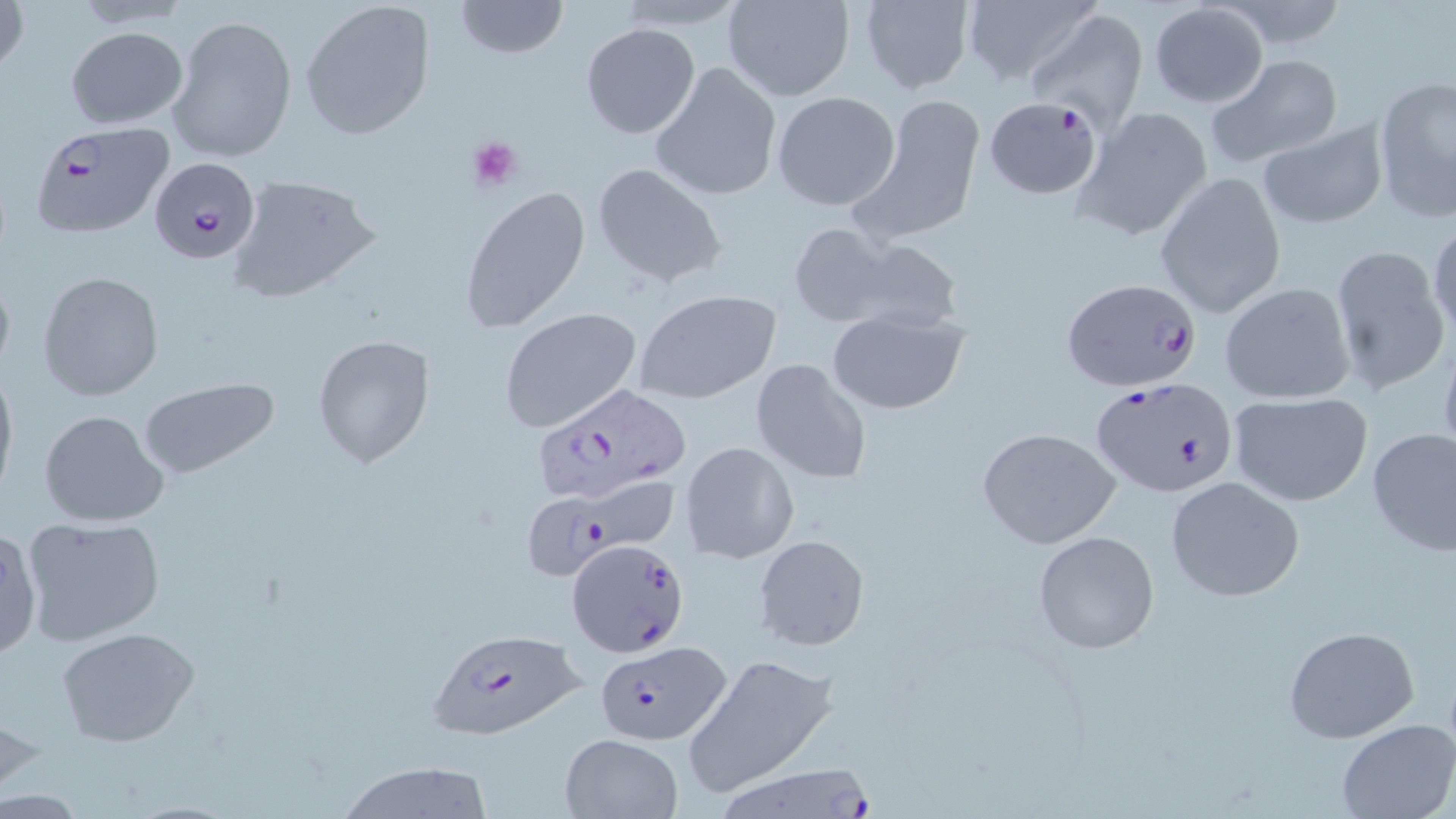
slide_level_diagnosis: Plasmodium falciparum
field_of_view: single
stain: May-Grünwald-Giemsa
image_size: 1456×819 pixels
plasmodium_falciparum_infected_red_blood_cell_locations: 'approximate bounding boxes as (x1, y1, x2, y2) in pixels: (983, 97, 1103, 200), (26, 122, 174, 240), (149, 157, 259, 264), (1060, 276, 1203, 392), (1089, 376, 1238, 498), (529, 385, 690, 506), (524, 482, 680, 590), (567, 539, 688, 659), (425, 628, 587, 741), (596, 641, 728, 741), (709, 764, 875, 818)'
magnification: 1000x
platelet_locations: 'approximate bounding boxes as (x1, y1, x2, y2) in pixels: (467, 134, 524, 193)'
preparation: thin blood smear
uninfected_red_blood_cell_locations: 'approximate bounding boxes as (x1, y1, x2, y2) in pixels: (0, 0, 29, 80), (298, 0, 438, 142), (722, 0, 855, 102), (858, 0, 975, 94), (959, 0, 1101, 89), (455, 1, 568, 58), (611, 2, 754, 33), (1147, 2, 1269, 108), (1027, 9, 1147, 127), (168, 15, 297, 162), (579, 23, 701, 139), (65, 26, 189, 130), (1205, 53, 1344, 168), (649, 61, 782, 202), (1371, 72, 1456, 225), (771, 91, 901, 212), (858, 96, 985, 238), (1073, 105, 1213, 240), (1256, 119, 1389, 232), (591, 163, 727, 289), (226, 172, 382, 305), (1156, 172, 1286, 320), (461, 184, 590, 334), (1428, 215, 1456, 342), (784, 221, 907, 329), (818, 233, 966, 335), (1329, 245, 1452, 398), (36, 270, 165, 402), (1217, 280, 1356, 405), (633, 288, 781, 401), (499, 307, 642, 433), (824, 309, 970, 415), (311, 333, 436, 468), (1436, 334, 1456, 467), (749, 357, 872, 485), (0, 360, 18, 501), (138, 377, 278, 479), (1227, 393, 1372, 505), (38, 409, 170, 528), (975, 426, 1122, 548), (1366, 427, 1455, 558), (679, 442, 798, 563), (1165, 477, 1305, 603), (20, 516, 166, 647), (0, 529, 41, 665), (1032, 529, 1160, 654), (753, 534, 870, 650), (1282, 625, 1421, 743), (58, 627, 199, 746), (682, 654, 834, 798), (1336, 720, 1456, 818), (558, 733, 685, 819), (334, 760, 494, 819)'
modality: light microscopy